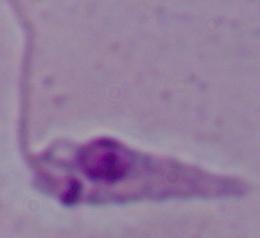
A Leishmania parasite is seen. Micrograph. Captured at 1000x magnification.